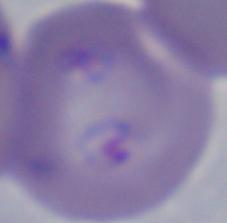 A Babesia parasite is shown. Captured at 1000x magnification. Micrograph.